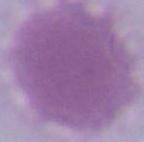
A red blood cell is seen. Photomicrograph. 1000x magnification.